Give the position of every Plasmodium parasite.
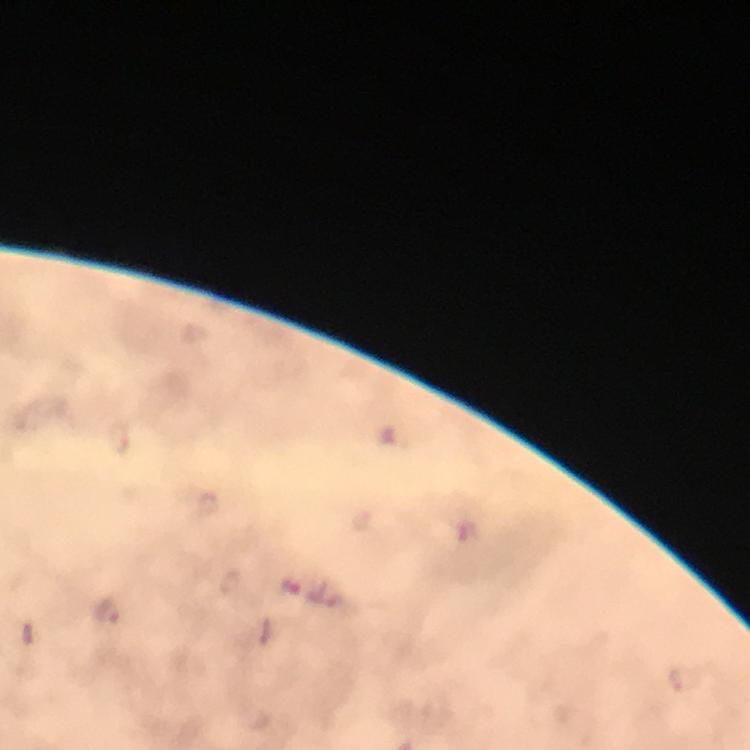
Approximate centers as {x, y} in pixels.
Plasmodium parasites: {119, 437}, {298, 587}, {107, 611}, {687, 680}.

Summary:
  - Context: from a diagnostic examination for malaria
  - Image size: 750×750 pixels
  - Immersion oil: applied
  - Preparation: thick smear
  - Magnification: 100x
  - Capture: smartphone mounted on the microscope
  - Stain: Giemsa
  - Cropped from: a single field of view